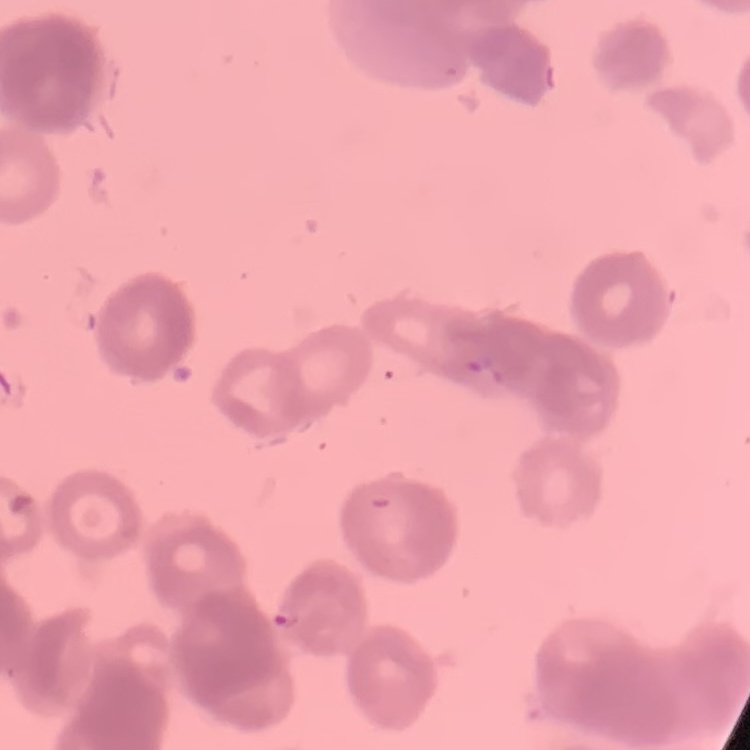 The erythrocytes show rouleaux formation. Square crop of a larger photomicrograph. Stained with either Field's or Giemsa. Thin blood smear.